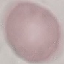

Summary:
  - Malaria status: uninfected
  - Image type: cell patch, automatically extracted from a larger field of view and resized to 64 × 64 pixels
  - Preparation: thin blood smear
  - Stain: Giemsa
  - Capture: smartphone through the microscope eyepiece